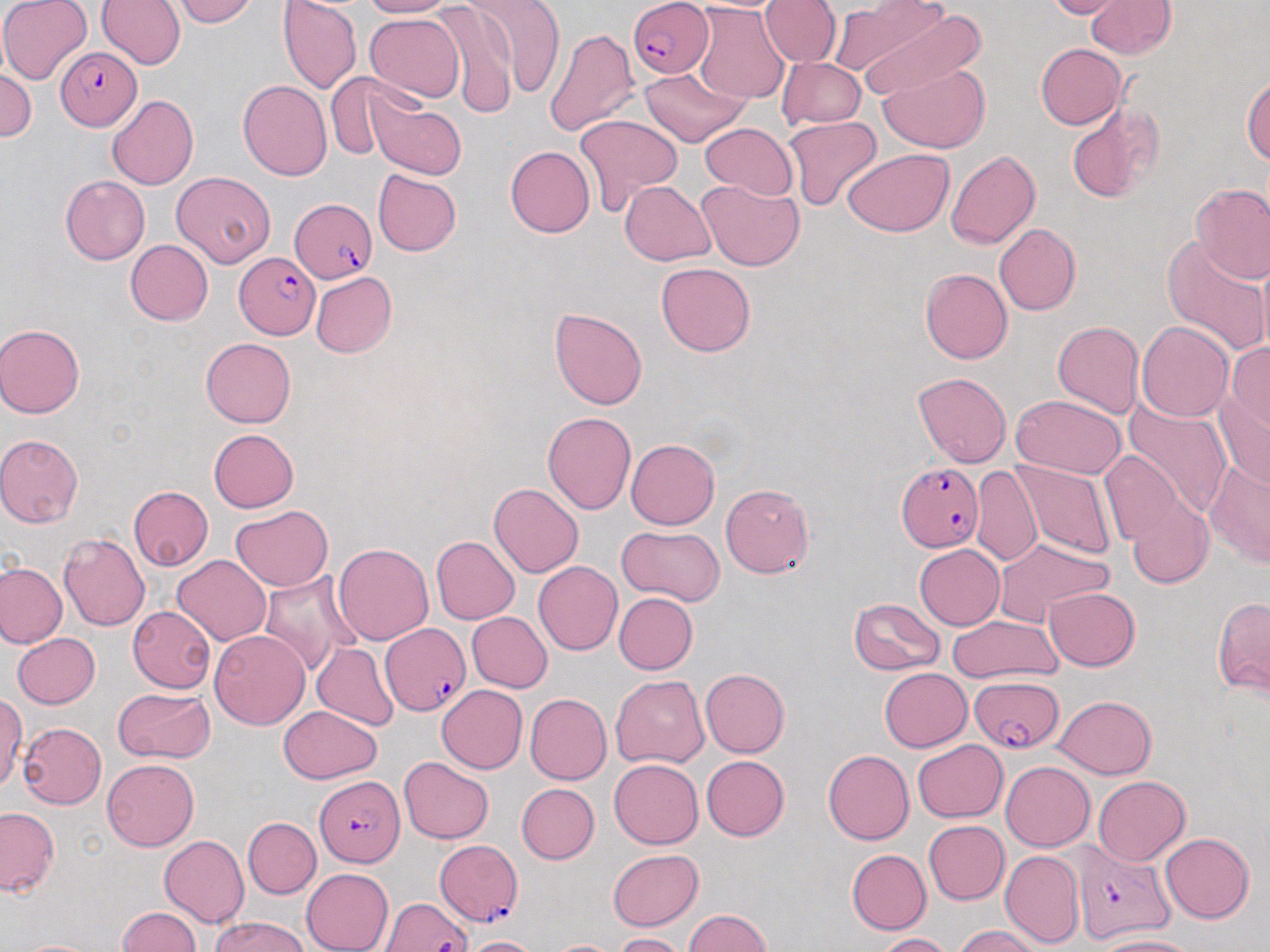
slide-level diagnosis = Plasmodium falciparum
modality = light microscopy
Plasmodium falciparum-infected red blood cell locations = approximate bounding boxes as (x1,y1)-(x2,y2) corner pairs in pixels: (627,0)-(712,79), (54,47)-(140,130), (290,198)-(378,283), (235,255)-(320,338), (898,461)-(982,549), (382,624)-(469,717), (970,676)-(1064,753), (315,776)-(405,868), (435,838)-(524,923), (1070,844)-(1173,944), (381,897)-(470,952)
field of view = single
magnification = 1000x
image size = 1270×952 pixels
preparation = thin blood film
stain = May-Grünwald-Giemsa
uninfected red blood cell locations = approximate bounding boxes as (x1,y1)-(x2,y2) corner pairs in pixels: (0,0)-(92,85), (97,0)-(187,69), (171,0)-(259,27), (360,0)-(457,18), (461,0)-(566,102), (760,0)-(841,68), (1046,0)-(1129,20), (1087,0)-(1176,59), (278,1)-(363,95), (429,2)-(518,117), (851,3)-(982,99), (692,4)-(790,104), (364,13)-(465,103), (544,29)-(639,137), (1035,43)-(1127,130), (776,57)-(865,130), (879,62)-(990,155), (638,67)-(750,148), (1,68)-(36,143), (326,71)-(406,159), (1243,77)-(1270,163), (238,79)-(332,181), (107,94)-(199,190), (371,95)-(463,180), (1066,102)-(1165,204), (575,114)-(683,214), (783,115)-(881,211), (701,122)-(797,200), (505,146)-(595,238), (843,149)-(954,237), (946,150)-(1039,249), (373,170)-(461,256), (171,172)-(275,267), (60,175)-(151,265), (620,179)-(714,263), (697,179)-(804,271), (1191,183)-(1270,283), (993,222)-(1080,315), (1161,234)-(1269,354), (125,240)-(213,325), (1257,250)-(1270,357), (656,262)-(756,357), (920,268)-(1013,363), (310,271)-(396,358), (550,308)-(647,409), (1052,320)-(1144,418), (1138,322)-(1234,421), (0,323)-(86,418), (201,337)-(296,427), (1225,342)-(1270,433), (912,371)-(1011,468), (1214,391)-(1270,488), (1010,394)-(1127,479), (1120,398)-(1234,517), (542,411)-(636,514), (208,429)-(299,512), (0,433)-(84,527), (625,438)-(718,530), (1099,451)-(1183,545), (1204,458)-(1270,569), (1012,461)-(1117,558), (972,465)-(1043,569), (489,482)-(583,578), (720,482)-(813,578), (128,486)-(213,570), (1127,495)-(1214,588), (230,504)-(333,591), (617,526)-(726,608), (58,531)-(150,631), (431,535)-(520,625), (993,537)-(1114,624), (334,543)-(434,645), (913,544)-(1005,630), (172,554)-(271,646), (533,560)-(623,655), (0,561)-(67,648), (258,571)-(360,675), (1043,587)-(1140,671), (613,592)-(697,674), (848,596)-(945,676), (1212,596)-(1270,698), (127,606)-(216,693), (467,612)-(552,692), (949,615)-(1062,682), (209,628)-(310,729), (11,633)-(100,709), (313,644)-(398,731), (879,667)-(972,752), (700,668)-(790,757), (611,675)-(708,768), (435,685)-(527,773), (113,687)-(215,764), (0,692)-(24,791), (524,693)-(612,785), (1054,695)-(1156,778), (277,706)-(382,783), (17,721)-(107,809), (913,740)-(1007,821), (822,750)-(915,845), (701,755)-(789,841), (400,756)-(494,843), (101,759)-(200,851), (608,759)-(703,849), (1001,761)-(1094,850), (1092,776)-(1190,866), (517,783)-(600,864), (0,807)-(59,897), (242,817)-(321,898), (924,820)-(1009,905), (1161,833)-(1255,923), (159,836)-(250,927), (607,849)-(703,930), (846,849)-(932,935), (999,849)-(1085,948), (301,868)-(394,952), (116,906)-(201,952), (685,909)-(770,952), (210,915)-(312,952), (953,925)-(1042,952), (615,933)-(688,952), (876,933)-(952,952), (461,936)-(543,952), (1096,936)-(1201,952), (11,938)-(107,952), (549,940)-(621,952)